Assess this cell for malaria.
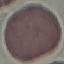

It is uninfected.

Cell patch, automatically extracted from a larger field of view and resized to 64 × 64 pixels. Giemsa stain. Photographed with a smartphone camera at the microscope eyepiece. Thin blood film.